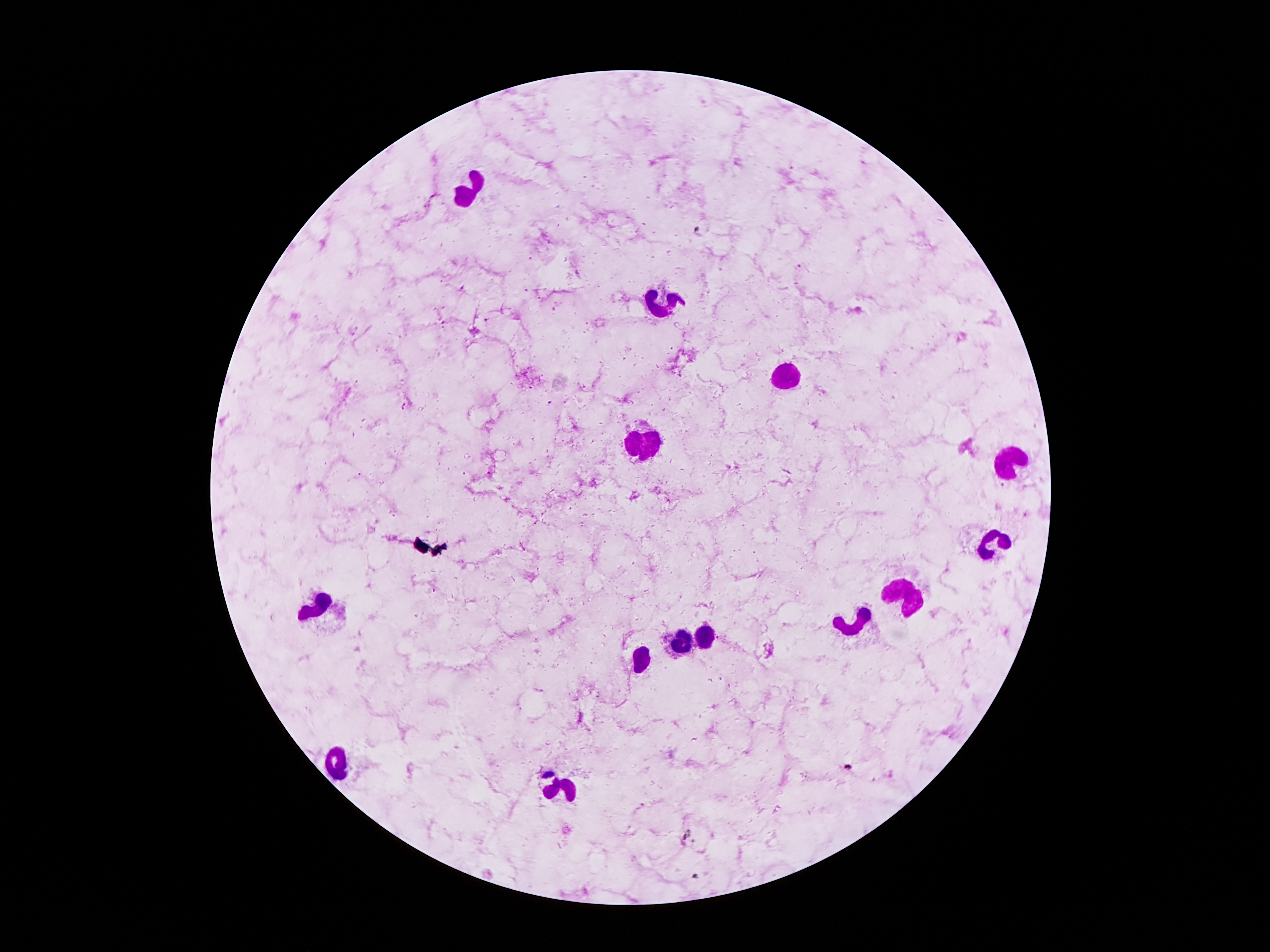
coordinate format = approximate centers as [x, y] in pixels
Plasmodium parasite locations = [551, 403], [403, 406]
leukocyte locations = [469, 193], [663, 304], [788, 379], [647, 443], [1011, 460], [994, 544], [903, 594], [316, 607], [850, 626], [707, 637], [685, 640], [642, 657], [337, 767], [561, 787]
patient malaria status = infected with Plasmodium falciparum
stain = Giemsa
image size = 1270×952 pixels
field of view = single
magnification = 100x
capture = smartphone camera through the microscope eyepiece
preparation = thick blood film